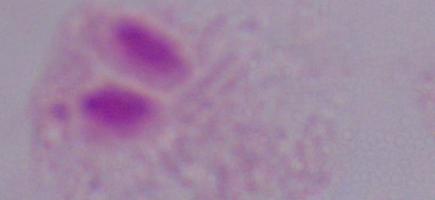

Photomicrograph. 1000x magnification. A trichomonad is shown.